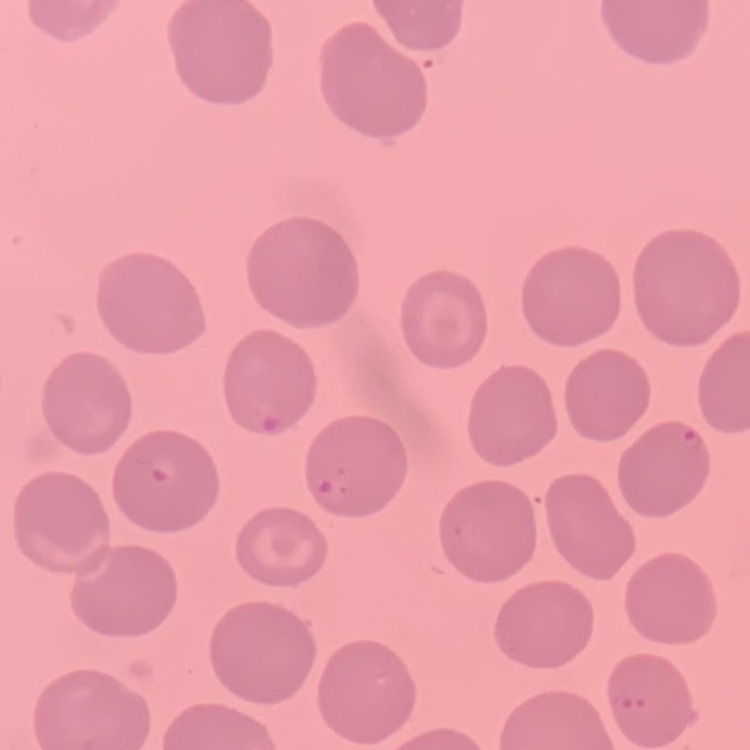

Summary:
  - Red blood cell morphology: no rouleaux formation
  - Stain: Field's or Giemsa
  - Preparation: thin blood smear
  - Image type: square crop of a larger photomicrograph